Assess the morphology of the red blood cells.
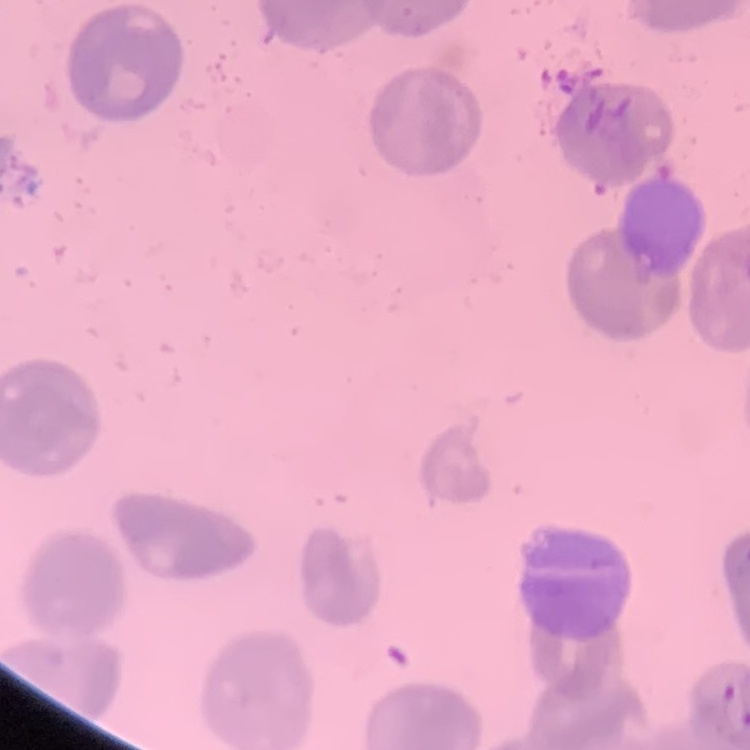

They show no rouleaux formation.

Summary:
  - Preparation: thin blood smear
  - Image type: one tile cut from a larger photomicrograph
  - Stain: Field's or Giemsa